Give the extent of all uninfected red blood cells.
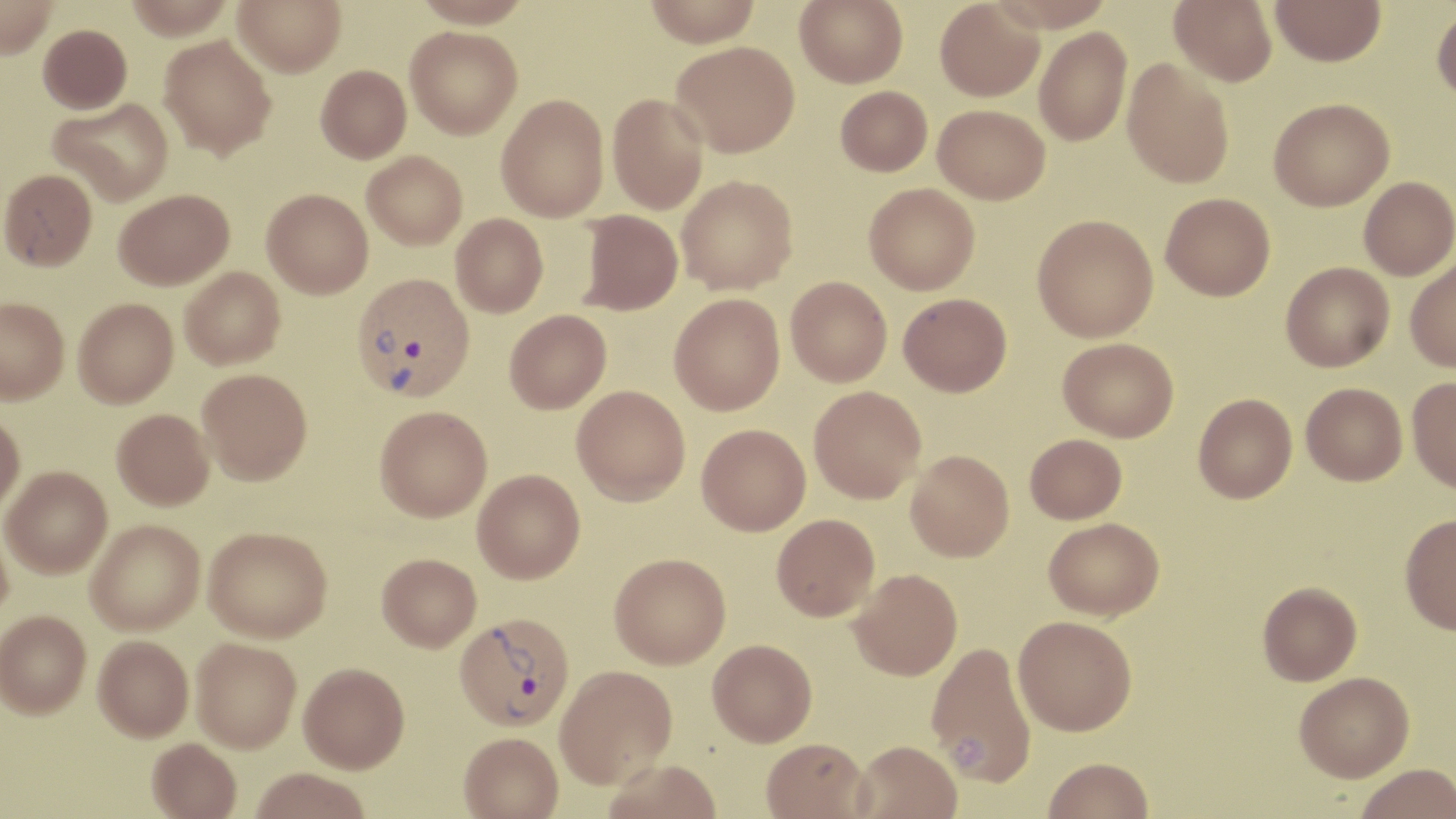
Approximate bounding boxes as named x1/y1/x2/y2 corners in pixels.
Uninfected red blood cells: (x1=0, y1=0, x2=58, y2=60), (x1=126, y1=0, x2=233, y2=41), (x1=232, y1=0, x2=346, y2=77), (x1=411, y1=0, x2=534, y2=28), (x1=643, y1=0, x2=762, y2=46), (x1=794, y1=0, x2=908, y2=87), (x1=934, y1=0, x2=1044, y2=101), (x1=987, y1=0, x2=1117, y2=32), (x1=1170, y1=0, x2=1277, y2=86), (x1=1270, y1=0, x2=1386, y2=66), (x1=1431, y1=5, x2=1456, y2=104), (x1=38, y1=24, x2=132, y2=114), (x1=405, y1=25, x2=522, y2=139), (x1=1034, y1=27, x2=1132, y2=146), (x1=159, y1=35, x2=277, y2=159), (x1=670, y1=40, x2=800, y2=157), (x1=1122, y1=59, x2=1235, y2=188), (x1=316, y1=64, x2=411, y2=163), (x1=835, y1=86, x2=932, y2=176), (x1=607, y1=93, x2=708, y2=214), (x1=496, y1=94, x2=609, y2=222), (x1=49, y1=97, x2=174, y2=206), (x1=1269, y1=98, x2=1394, y2=211), (x1=933, y1=104, x2=1050, y2=204), (x1=362, y1=151, x2=467, y2=250), (x1=0, y1=169, x2=97, y2=270), (x1=676, y1=175, x2=798, y2=295), (x1=1359, y1=176, x2=1456, y2=280), (x1=864, y1=182, x2=980, y2=295), (x1=262, y1=188, x2=373, y2=298), (x1=114, y1=189, x2=234, y2=289), (x1=1160, y1=192, x2=1275, y2=300), (x1=579, y1=210, x2=682, y2=315), (x1=451, y1=213, x2=548, y2=317), (x1=1032, y1=214, x2=1158, y2=342), (x1=1405, y1=257, x2=1456, y2=372), (x1=1281, y1=262, x2=1394, y2=371), (x1=180, y1=267, x2=285, y2=369), (x1=786, y1=276, x2=892, y2=386), (x1=899, y1=292, x2=1012, y2=396), (x1=669, y1=293, x2=785, y2=415), (x1=0, y1=297, x2=70, y2=404), (x1=73, y1=297, x2=178, y2=408), (x1=505, y1=309, x2=611, y2=413), (x1=1058, y1=337, x2=1179, y2=442), (x1=197, y1=368, x2=312, y2=484), (x1=1407, y1=376, x2=1456, y2=494), (x1=1301, y1=382, x2=1407, y2=485), (x1=572, y1=386, x2=690, y2=505), (x1=809, y1=386, x2=926, y2=503), (x1=1193, y1=393, x2=1297, y2=503), (x1=374, y1=405, x2=492, y2=521), (x1=112, y1=408, x2=214, y2=510), (x1=0, y1=411, x2=25, y2=517), (x1=697, y1=424, x2=811, y2=535), (x1=1025, y1=433, x2=1127, y2=523), (x1=906, y1=450, x2=1014, y2=561), (x1=2, y1=466, x2=112, y2=578), (x1=473, y1=469, x2=585, y2=583), (x1=772, y1=514, x2=879, y2=620), (x1=1400, y1=514, x2=1456, y2=635), (x1=1043, y1=517, x2=1164, y2=620), (x1=86, y1=519, x2=204, y2=636), (x1=0, y1=522, x2=13, y2=629), (x1=203, y1=526, x2=332, y2=642), (x1=377, y1=553, x2=481, y2=651), (x1=609, y1=553, x2=731, y2=668), (x1=849, y1=568, x2=962, y2=680), (x1=1257, y1=581, x2=1362, y2=685), (x1=0, y1=611, x2=91, y2=721), (x1=1013, y1=615, x2=1137, y2=736), (x1=93, y1=638, x2=194, y2=744), (x1=708, y1=638, x2=817, y2=746), (x1=191, y1=640, x2=301, y2=754), (x1=926, y1=641, x2=1037, y2=787), (x1=299, y1=664, x2=410, y2=776), (x1=555, y1=664, x2=677, y2=789), (x1=1294, y1=671, x2=1414, y2=781), (x1=459, y1=732, x2=564, y2=819), (x1=761, y1=737, x2=871, y2=818), (x1=853, y1=740, x2=963, y2=819), (x1=146, y1=741, x2=241, y2=819), (x1=1042, y1=757, x2=1154, y2=818), (x1=600, y1=758, x2=723, y2=819), (x1=1355, y1=763, x2=1456, y2=819), (x1=250, y1=771, x2=370, y2=819).

Summary:
  - Plasmodium vivax-infected red blood cell locations: (x1=351, y1=272, x2=474, y2=401), (x1=455, y1=612, x2=575, y2=731)
  - Slide-level diagnosis: Plasmodium vivax
  - Field of view: one of a larger specimen
  - Preparation: thin blood smear
  - Magnification: 1000x
  - Modality: optical microscopy
  - Image size: 1456×819 pixels
  - Stain: May-Grünwald-Giemsa